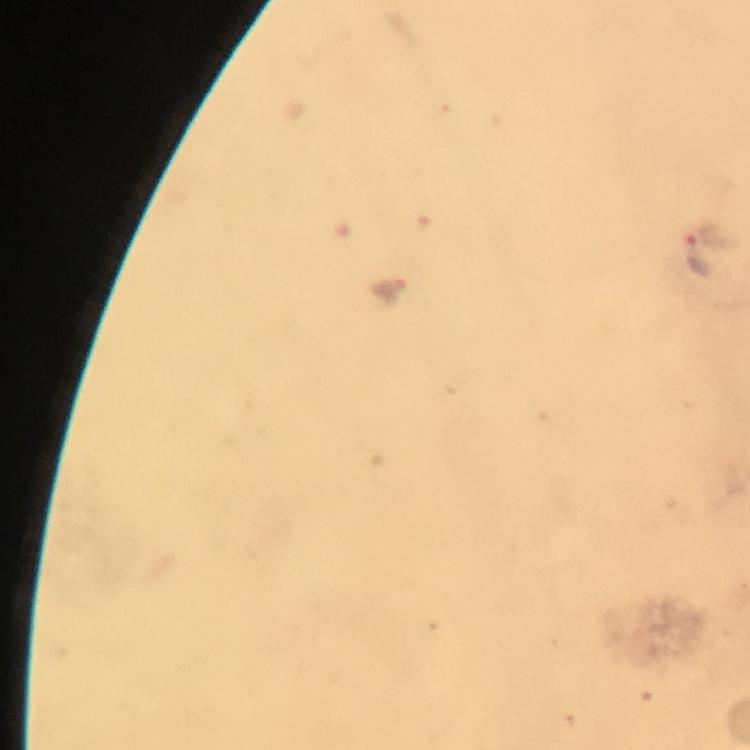
magnification = 100x
immersion oil = used
capture = smartphone mounted on the microscope
stain = Giemsa
Plasmodium parasite locations = approximate centers as [x, y] in pixels: [700, 255]
cropped from = one field of view
preparation = thick blood smear
image size = 750×750 pixels
context = from a diagnostic examination for malaria